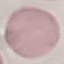

Summary:
  - Result: negative for malaria parasites
  - Preparation: thin blood film
  - Stain: Giemsa
  - Capture: smartphone through the microscope eyepiece
  - Image type: automatically extracted cell patch, resized to 64 × 64 pixels